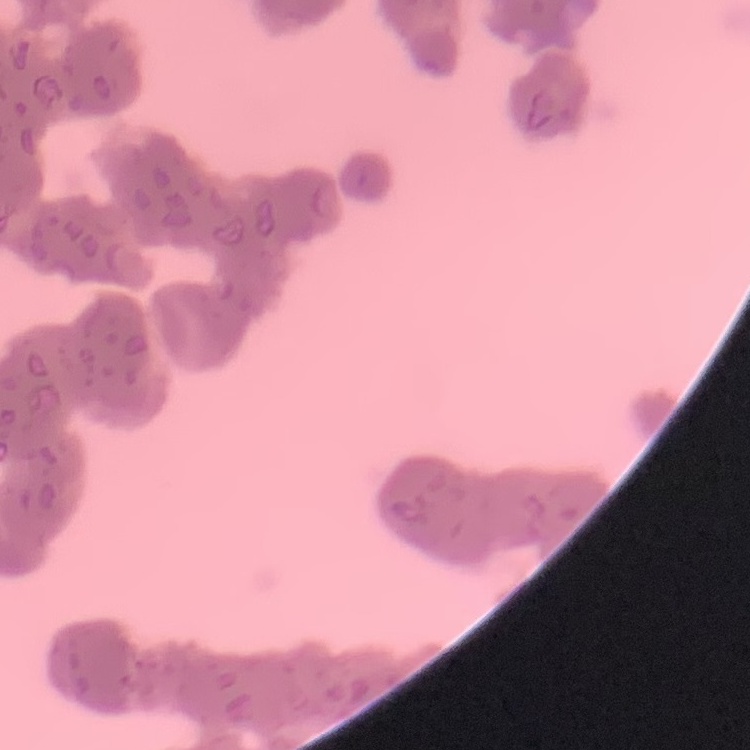

The erythrocytes exhibit rouleaux formation. Thin peripheral smear. One tile cut from a larger photomicrograph. Stained with either Field's or Giemsa.